Identify the parasite.
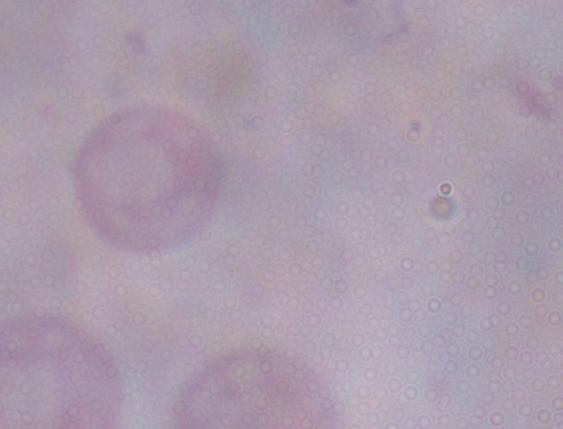

This is a trypanosome.

magnification: 1000x
modality: micrograph